Identify the parasite.
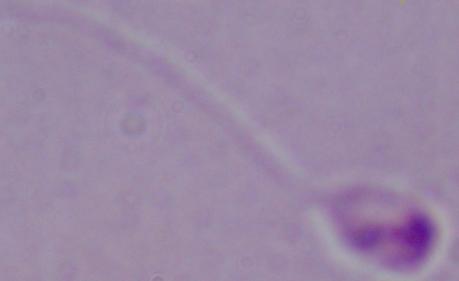
Leishmania.

Summary:
  - Modality: micrograph
  - Magnification: 1000x